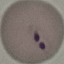
Malaria status: parasitized. Thin blood film. Cell patch, automatically extracted from a larger field of view and resized to 64 × 64 pixels. Giemsa stain. Photographed with a smartphone camera at the microscope eyepiece.